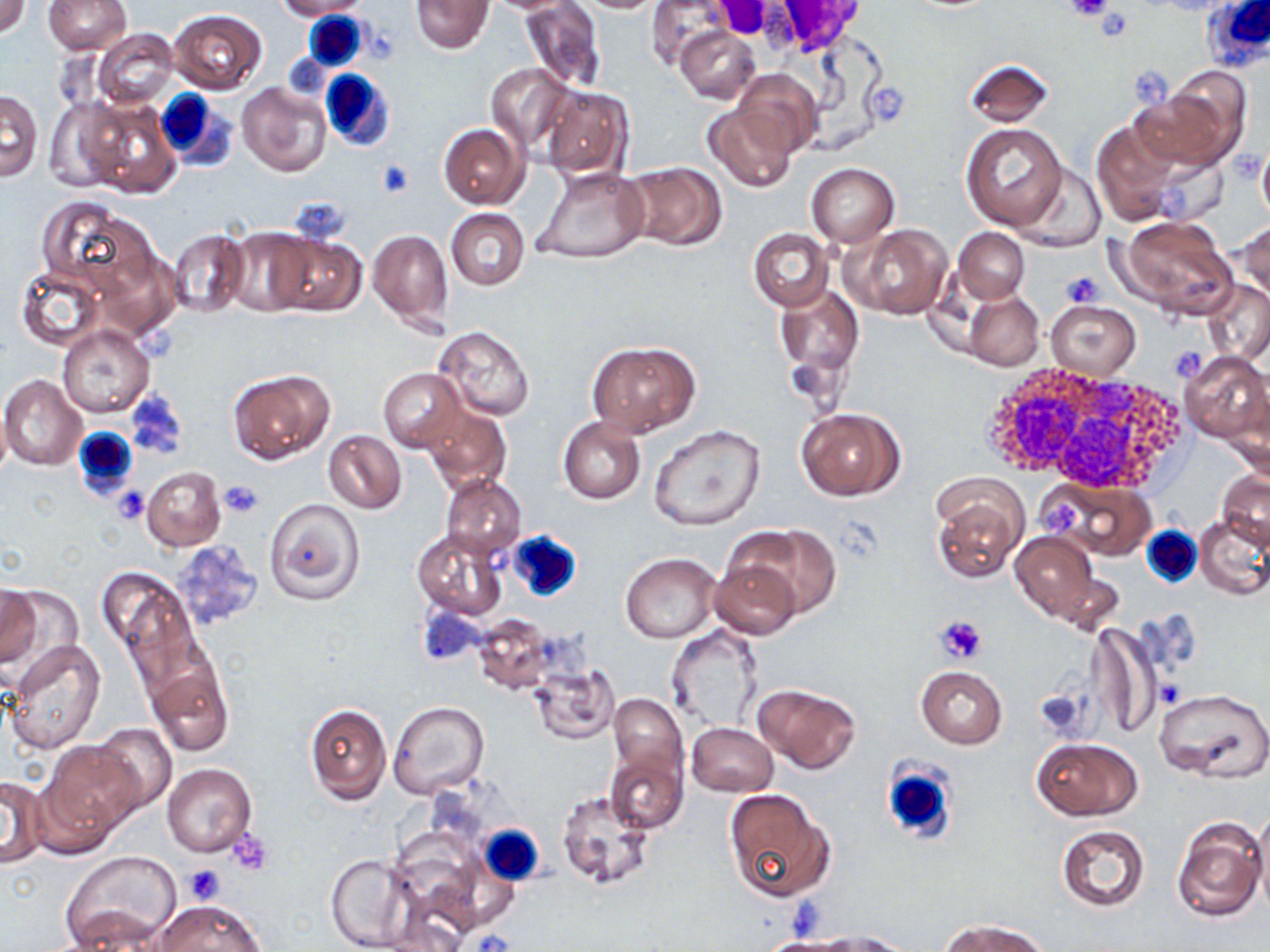
slide-level diagnosis = no evidence of blood parasites
preparation = thin blood film
image size = 1270×952 pixels
modality = optical microscopy
platelet locations = approximate bounding boxes as [x1, y1, x2, y2] in pixels: [1067, 0, 1115, 22], [1093, 11, 1133, 39], [865, 80, 913, 126], [374, 159, 415, 197], [1060, 270, 1103, 307], [1168, 344, 1208, 383], [219, 480, 264, 519], [113, 486, 150, 525], [935, 615, 987, 666], [1156, 678, 1183, 708], [1035, 688, 1091, 740], [228, 829, 273, 874], [182, 864, 225, 905], [474, 929, 514, 952]
magnification = 1000x
uninfected red blood cell locations = approximate bounding boxes as [x1, y1, x2, y2] in pixels: [0, 0, 31, 38], [278, 0, 371, 18], [412, 0, 492, 53], [572, 0, 670, 13], [646, 0, 731, 71], [43, 1, 132, 54], [519, 1, 606, 94], [169, 10, 267, 94], [676, 26, 760, 103], [92, 28, 179, 109], [964, 59, 1054, 127], [485, 63, 574, 152], [734, 68, 821, 156], [236, 82, 330, 177], [539, 85, 632, 178], [1129, 85, 1238, 177], [1, 90, 42, 181], [42, 96, 128, 192], [82, 98, 180, 199], [703, 102, 798, 192], [1091, 120, 1184, 227], [438, 123, 529, 209], [961, 123, 1068, 230], [1010, 161, 1106, 252], [621, 163, 727, 251], [806, 163, 899, 246], [534, 167, 651, 264], [39, 197, 158, 303], [446, 209, 529, 290], [1113, 215, 1239, 320], [1235, 220, 1269, 305], [848, 224, 952, 320], [224, 228, 317, 316], [953, 228, 1030, 302], [167, 229, 250, 320], [750, 229, 832, 310], [368, 230, 453, 330], [267, 234, 366, 318], [14, 265, 105, 351], [1202, 280, 1269, 364], [776, 283, 864, 377], [963, 289, 1043, 371], [1044, 300, 1140, 380], [59, 325, 153, 417], [433, 327, 535, 421], [588, 341, 699, 437], [1179, 351, 1268, 442], [228, 368, 335, 465], [378, 369, 465, 450], [1, 374, 86, 470], [1225, 382, 1270, 480], [420, 402, 512, 494], [795, 406, 905, 501], [559, 417, 645, 503], [649, 425, 766, 533], [322, 429, 409, 514], [141, 466, 226, 551], [1216, 470, 1270, 548], [440, 475, 527, 557], [1041, 479, 1156, 560], [931, 486, 1026, 586], [263, 498, 366, 605], [1194, 513, 1270, 599], [732, 525, 841, 619], [412, 529, 507, 618], [1009, 530, 1100, 622], [169, 541, 263, 633], [622, 553, 719, 643], [708, 557, 804, 640], [1048, 564, 1127, 637], [98, 566, 194, 673], [0, 586, 41, 667], [472, 613, 556, 695], [1088, 621, 1159, 742], [666, 625, 764, 732], [6, 640, 107, 755], [146, 660, 233, 757], [528, 665, 618, 744], [916, 665, 1007, 748], [752, 683, 861, 773], [1154, 686, 1270, 783], [608, 692, 688, 791], [389, 702, 489, 799], [303, 703, 390, 805], [89, 722, 178, 815], [686, 723, 777, 797], [1034, 738, 1142, 819], [40, 742, 140, 844], [605, 746, 689, 835], [162, 764, 256, 856], [0, 773, 47, 868], [555, 787, 655, 894], [724, 790, 833, 902], [1252, 806, 1270, 914], [1172, 816, 1266, 922], [1056, 824, 1151, 912], [62, 851, 181, 950], [324, 852, 419, 952], [152, 899, 265, 952], [64, 904, 172, 949], [945, 919, 1047, 952], [818, 931, 910, 951]
stain = May-Grünwald-Giemsa
white blood cell locations = approximate bounding boxes as [x1, y1, x2, y2] in pixels: [1201, 0, 1270, 71], [297, 13, 369, 74], [318, 67, 397, 153], [153, 89, 237, 171], [973, 365, 1190, 489], [71, 425, 140, 501], [1141, 526, 1201, 588], [506, 530, 584, 602], [882, 763, 957, 845], [478, 824, 545, 885]
field of view = one of a larger specimen